Assess this cell for malaria.
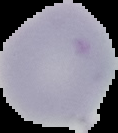
Uninfected.

Summary:
  - Preparation: thin blood smear
  - Image type: segmented cell region on a black background
  - Image size: 118×133 pixels